Assess the morphology of the erythrocytes.
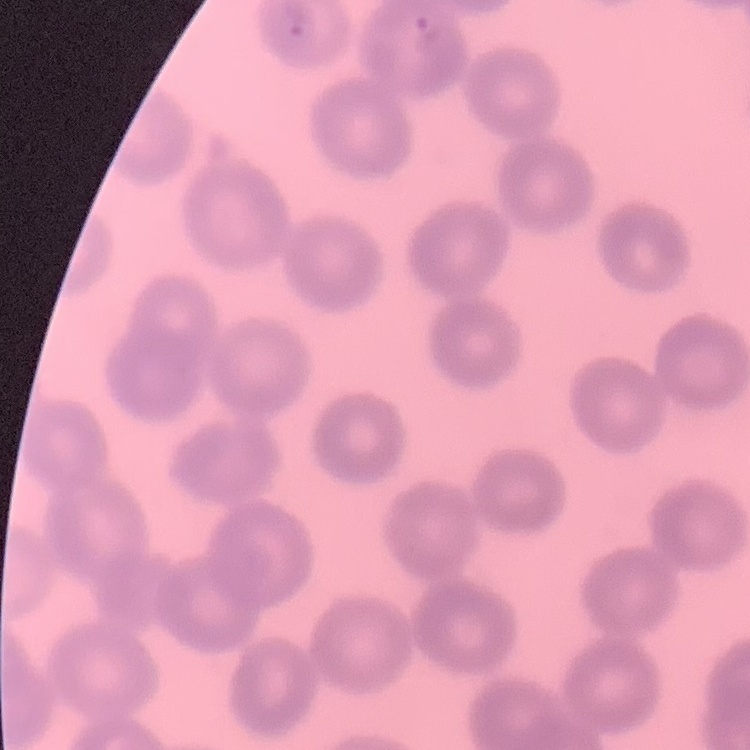

No rouleaux formation.

stain = Field's or Giemsa
image type = square crop of a larger photomicrograph
preparation = thin blood film